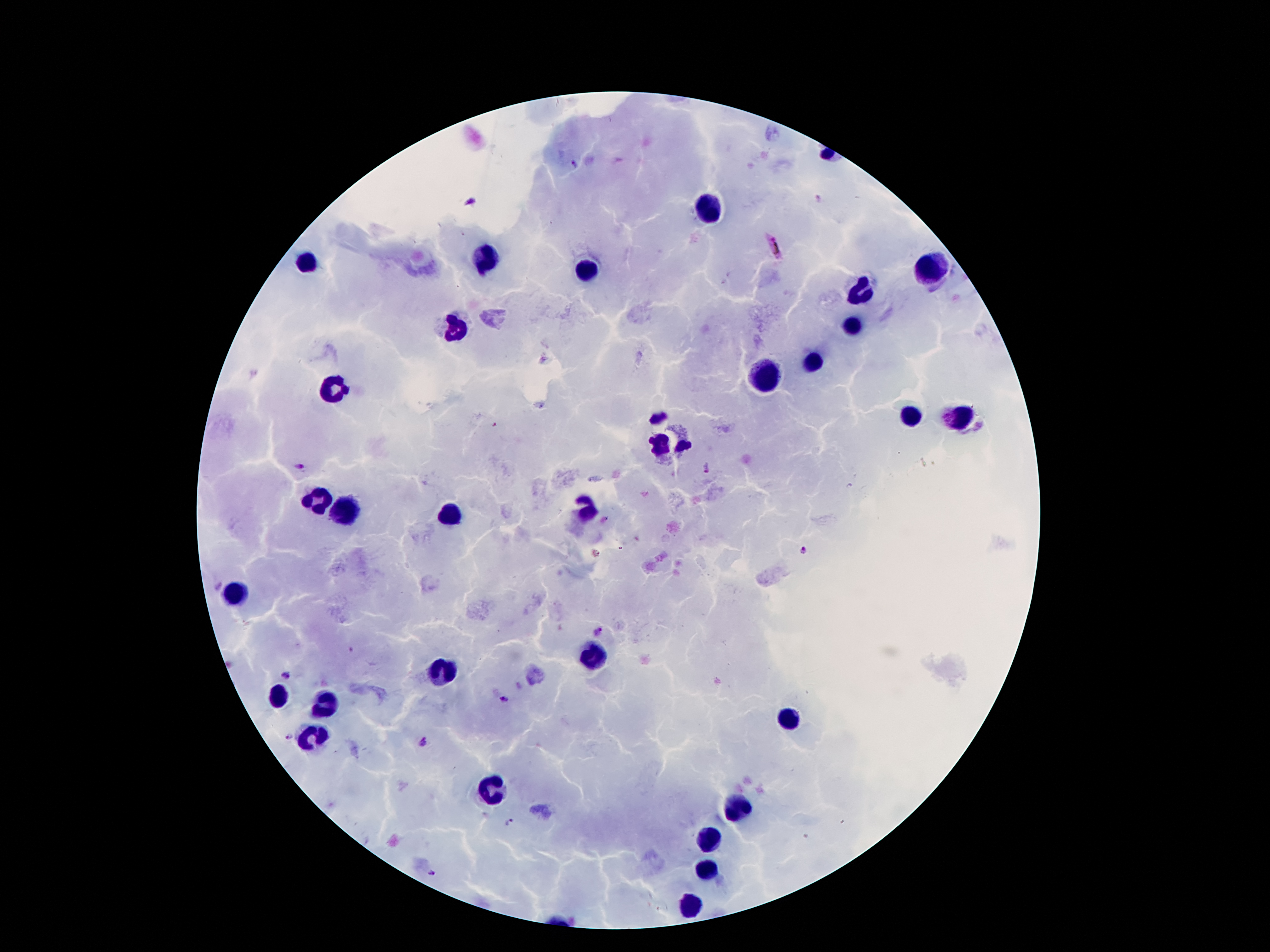

Approximate centers as [x, y] in pixels.
Summary:
  - Leukocyte locations: [706, 209], [483, 255], [306, 266], [930, 268], [589, 270], [861, 293], [852, 326], [459, 330], [812, 361], [762, 374], [332, 385], [910, 414], [956, 416], [662, 438], [315, 500], [587, 509], [344, 516], [454, 518], [237, 591], [593, 657], [441, 675], [277, 695], [324, 704], [786, 724], [313, 737], [494, 794], [735, 812], [706, 841], [704, 872], [689, 905]
  - Plasmodium parasite locations: [573, 163], [819, 199], [774, 244], [299, 466], [708, 467], [805, 551], [599, 633], [286, 673], [505, 701], [292, 736], [423, 742], [508, 821], [432, 874]
  - Patient malaria status: infected with Plasmodium falciparum
  - Capture: smartphone camera through the microscope eyepiece
  - Image size: 1270×952 pixels
  - Stain: Giemsa
  - Magnification: 100x
  - Field of view: one from this slide
  - Preparation: thick peripheral-blood smear